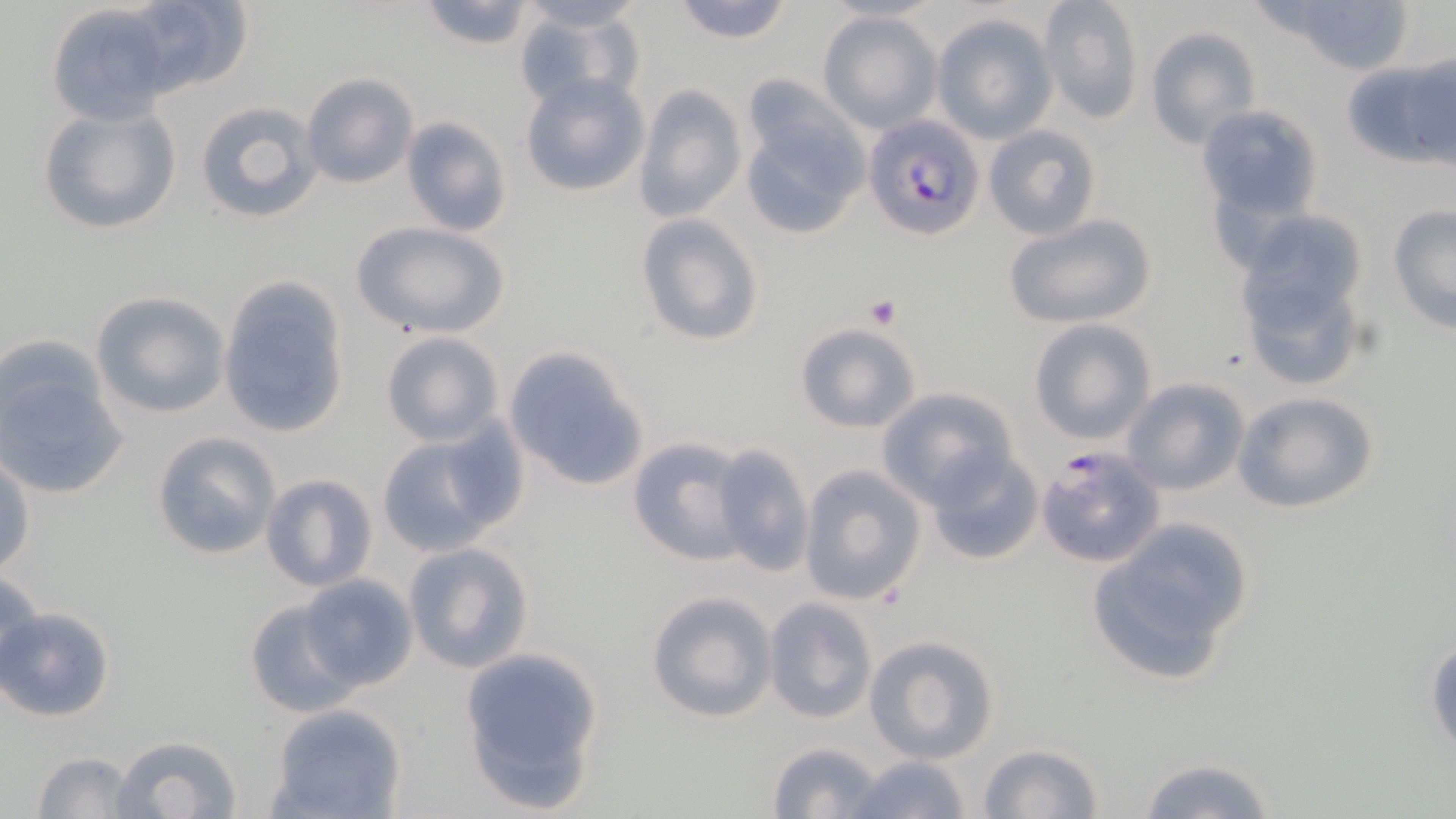
Summary:
  - Coordinate format: approximate bounding boxes as [x1, y1, x2, y2] in pixels
  - Platelet locations: [864, 297, 901, 329]
  - Uninfected red blood cell locations: [669, 0, 796, 45], [1039, 0, 1144, 125], [1261, 0, 1419, 76], [122, 1, 255, 98], [414, 1, 542, 50], [512, 1, 647, 35], [46, 4, 177, 125], [511, 5, 646, 112], [818, 11, 942, 133], [931, 14, 1057, 142], [1143, 26, 1261, 149], [1344, 52, 1452, 170], [299, 72, 418, 189], [520, 73, 650, 198], [632, 83, 748, 223], [738, 86, 870, 241], [193, 100, 325, 225], [38, 103, 182, 236], [1195, 103, 1323, 228], [401, 116, 513, 237], [982, 124, 1101, 240], [1388, 204, 1455, 334], [1004, 212, 1158, 330], [635, 214, 764, 347], [348, 221, 510, 338], [1230, 225, 1374, 395], [217, 276, 350, 439], [91, 291, 229, 418], [1028, 319, 1157, 444], [793, 321, 922, 434], [378, 330, 504, 446], [0, 338, 130, 501], [502, 346, 653, 494], [1123, 377, 1250, 496], [875, 388, 1015, 507], [1231, 390, 1381, 515], [374, 426, 515, 557], [151, 431, 281, 561], [627, 436, 753, 567], [709, 442, 815, 578], [923, 447, 1044, 567], [0, 452, 35, 579], [797, 464, 925, 607], [259, 473, 377, 592], [1085, 520, 1254, 687], [401, 542, 534, 675], [0, 570, 47, 686], [298, 575, 417, 692], [645, 589, 778, 722], [244, 597, 356, 714], [763, 597, 878, 724], [2, 604, 116, 722], [864, 635, 1000, 762], [1426, 639, 1456, 757], [458, 646, 607, 814], [268, 703, 406, 818], [108, 734, 243, 819], [767, 739, 886, 818], [977, 743, 1105, 818], [31, 751, 143, 818], [845, 754, 975, 818], [1133, 754, 1279, 819]
  - Plasmodium falciparum-infected red blood cell locations: [866, 115, 985, 241], [1034, 445, 1167, 570]
  - Slide-level diagnosis: Plasmodium falciparum
  - Stain: May-Grünwald-Giemsa
  - Field of view: one of a larger specimen
  - Image size: 1456×819 pixels
  - Modality: optical microscopy
  - Magnification: 1000x
  - Preparation: thin blood smear